Assess the morphology of the red blood cells.
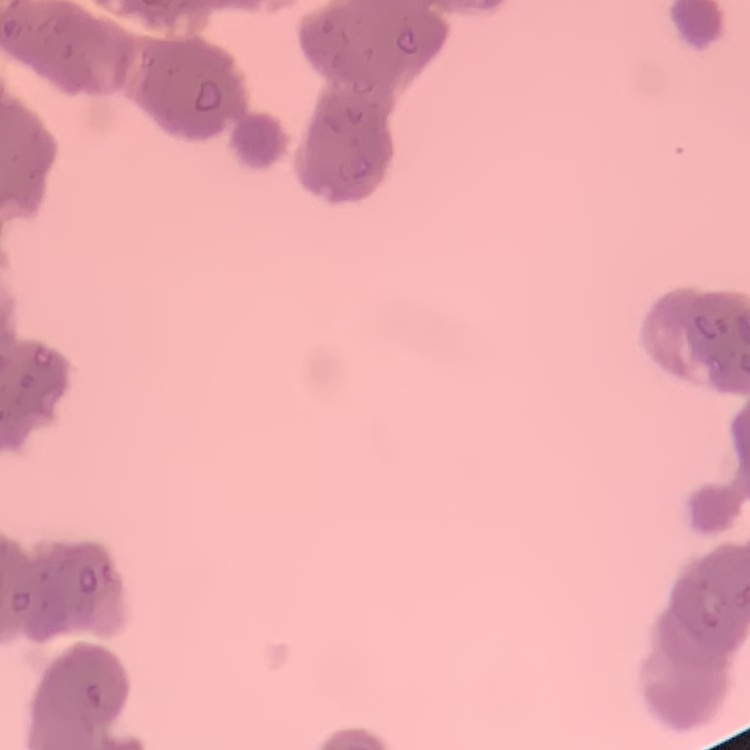

They show rouleaux formation.

Field's or Giemsa stain. Thin blood film. Square crop of a larger photomicrograph.